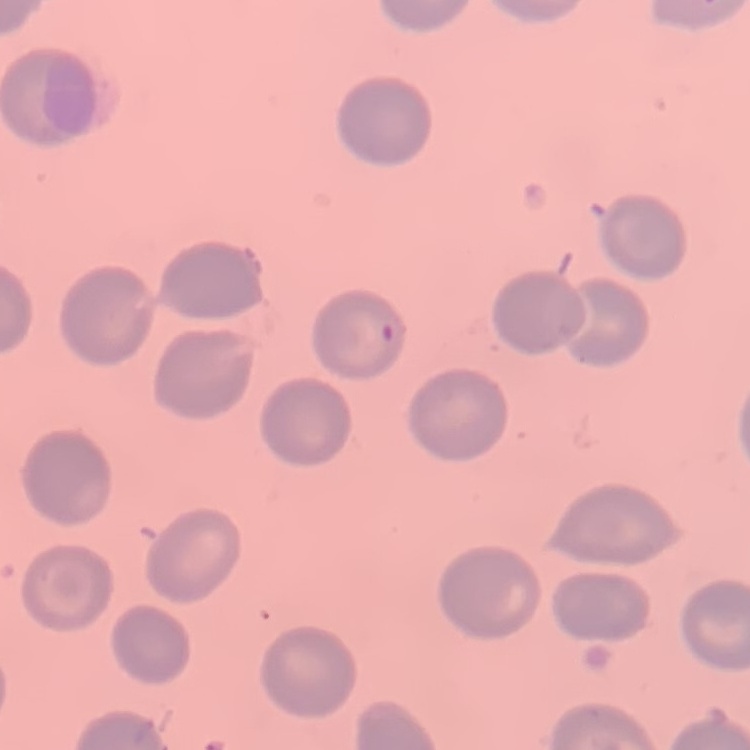

The erythrocytes show no rouleaux formation. Square crop of a larger photomicrograph. Stained with either Field's or Giemsa. Thin blood film.